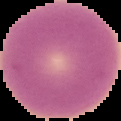

{
  "image_type": "segmented cell region with the area outside set to black",
  "image_size": "121×121 pixels",
  "result": "negative for Plasmodium parasites",
  "preparation": "thin blood smear"
}